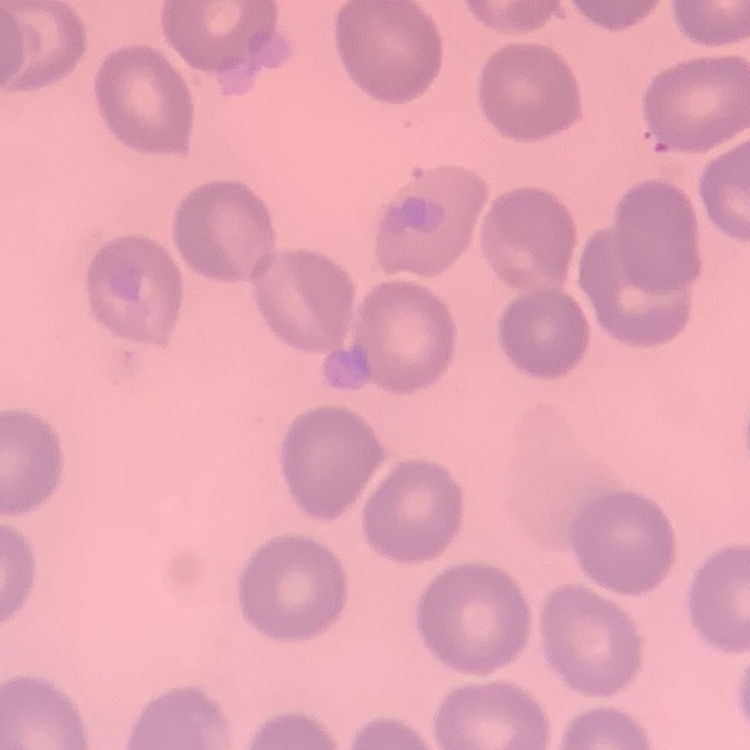

The erythrocytes show no rouleaux formation. Square crop of a larger photomicrograph. Thin peripheral smear. Stained with either Field's or Giemsa.